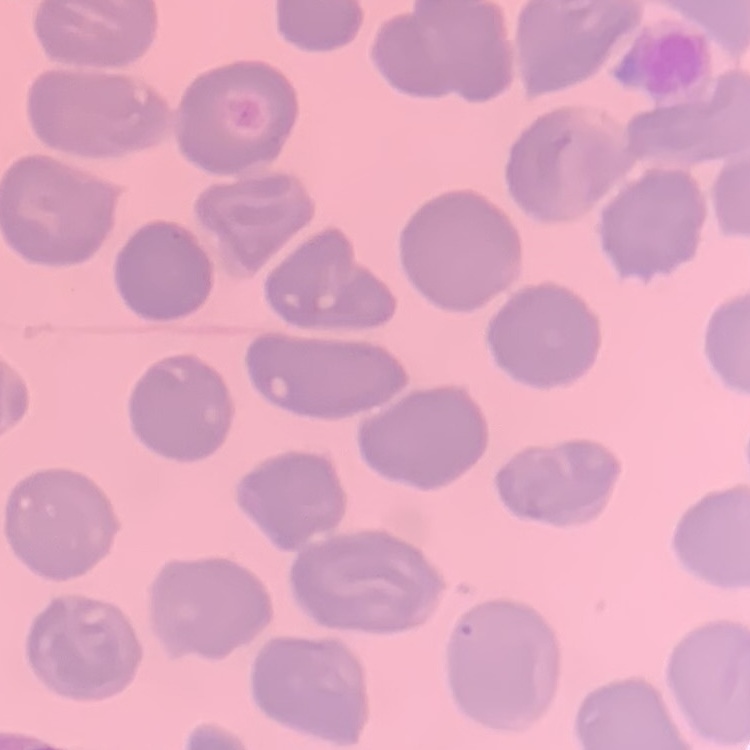
red_blood_cell_morphology: no rouleaux formation
preparation: thin blood film
stain: Field's or Giemsa
image_type: one tile cut from a larger photomicrograph